Assess this cell for malaria.
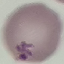

Uninfected.

{
  "stain": "Giemsa",
  "image_type": "cell patch, automatically extracted from a larger field of view and resized to 64 × 64 pixels",
  "capture": "smartphone through the microscope eyepiece",
  "preparation": "thin smear"
}